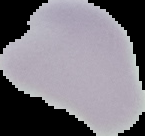
Summary:
  - Image type: cell region segmented out of the field of view; surrounding area masked to black
  - Image size: 145×136 pixels
  - Result: negative for malaria parasites
  - Preparation: thin blood film